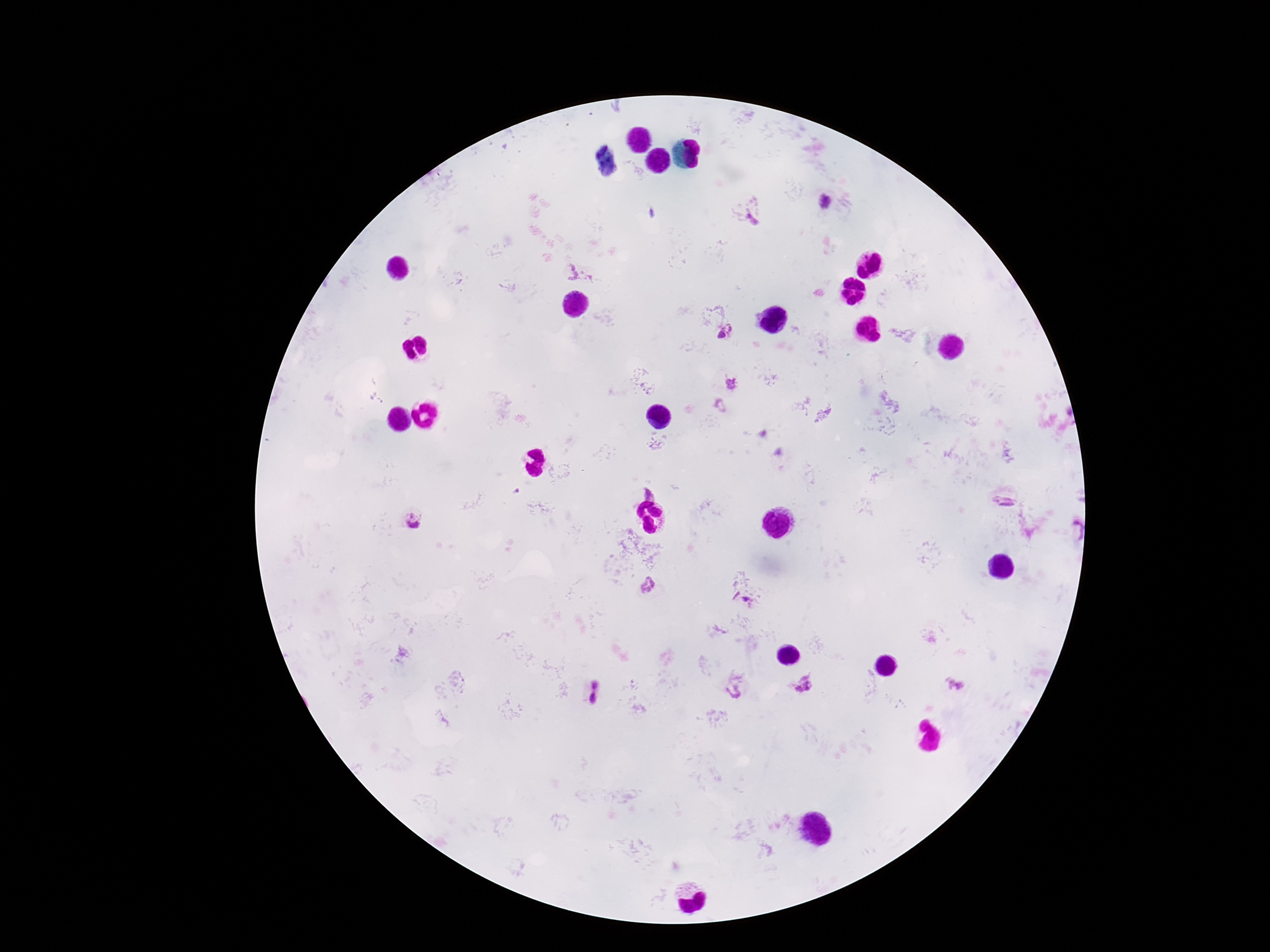

Approximate centers as [x, y] in pixels.
Summary:
  - Plasmodium parasite locations: [823, 203], [749, 217], [579, 272], [726, 334], [731, 384], [648, 494], [1002, 502], [414, 520], [1073, 532], [648, 586], [742, 600], [595, 684], [803, 684], [955, 685], [734, 690], [593, 697]
  - Image size: 1270×952 pixels
  - Magnification: 100x
  - Field of view: one from this slide
  - Patient malaria status: positive
  - Preparation: thick peripheral-blood smear
  - Stain: Giemsa
  - Capture: smartphone camera through the microscope eyepiece